Name the parasite shown.
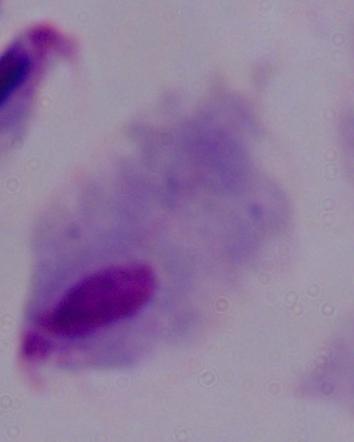

A trichomonad.

Summary:
  - Modality: photomicrograph
  - Magnification: 1000x